Outline each uninfected red blood cell.
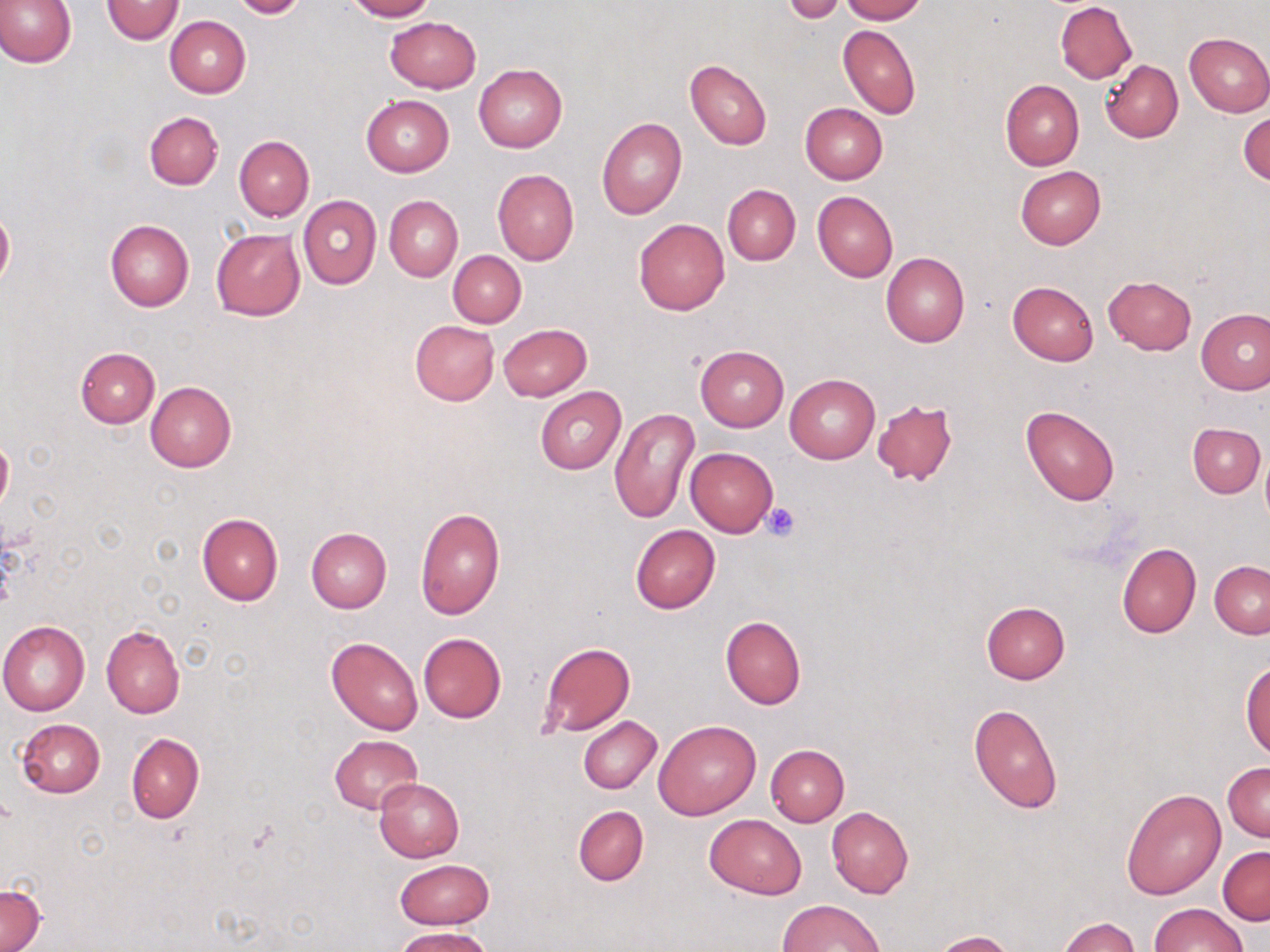
Approximate bounding boxes as (x1,y1)-(x2,y2) corner pairs in pixels.
Uninfected red blood cells: (0,0)-(75,68), (102,0)-(185,45), (229,0)-(309,19), (343,0)-(435,21), (839,0)-(927,23), (783,1)-(846,23), (1055,2)-(1136,83), (165,16)-(250,97), (384,16)-(481,93), (838,24)-(920,119), (1183,32)-(1270,117), (685,60)-(771,150), (1100,60)-(1183,142), (474,65)-(568,152), (1000,79)-(1083,170), (361,95)-(454,176), (800,103)-(888,184), (144,111)-(223,190), (1239,112)-(1269,187), (597,117)-(686,219), (234,136)-(313,221), (1015,166)-(1106,248), (492,169)-(578,265), (722,185)-(800,265), (812,191)-(898,282), (298,195)-(381,290), (384,195)-(463,282), (0,206)-(14,293), (634,217)-(730,314), (105,218)-(194,311), (211,228)-(305,320), (449,250)-(526,328), (881,251)-(969,346), (1103,275)-(1197,354), (1007,280)-(1099,366), (1197,310)-(1270,395), (410,321)-(499,405), (498,323)-(591,401), (696,345)-(788,431), (74,346)-(159,427), (784,372)-(880,464), (146,381)-(236,471), (535,387)-(626,474), (872,399)-(959,487), (1021,405)-(1120,505), (610,407)-(701,526), (1188,422)-(1265,497), (0,438)-(13,511), (686,448)-(777,536), (1260,450)-(1270,528), (415,508)-(506,621), (197,513)-(283,606), (630,525)-(720,613), (306,527)-(392,612), (1117,543)-(1201,638), (1209,561)-(1270,637), (981,601)-(1070,683), (721,617)-(806,709), (0,620)-(90,715), (102,624)-(185,718), (418,633)-(506,723), (326,637)-(423,736), (538,642)-(634,736), (1241,661)-(1270,759), (968,701)-(1063,813), (578,716)-(662,794), (16,719)-(105,798), (653,719)-(761,820), (126,732)-(203,823), (329,735)-(422,815), (766,745)-(849,826), (1223,761)-(1269,841), (373,777)-(465,862), (1121,787)-(1226,900), (573,806)-(648,885), (826,807)-(913,898), (704,814)-(806,897), (1217,846)-(1269,924), (393,858)-(493,929), (1,882)-(45,951), (779,899)-(884,951), (1150,902)-(1246,952), (1058,917)-(1138,952), (395,927)-(494,952), (932,930)-(1016,952).

Platelet locations: (764,501)-(803,541). Slide-level diagnosis: no evidence of blood parasites. One field of a larger specimen. Optical microscopy. Image is 1270×952 pixels. May-Grünwald-Giemsa stain. Thin blood film. 1000x magnification.